Point out each leukocyte.
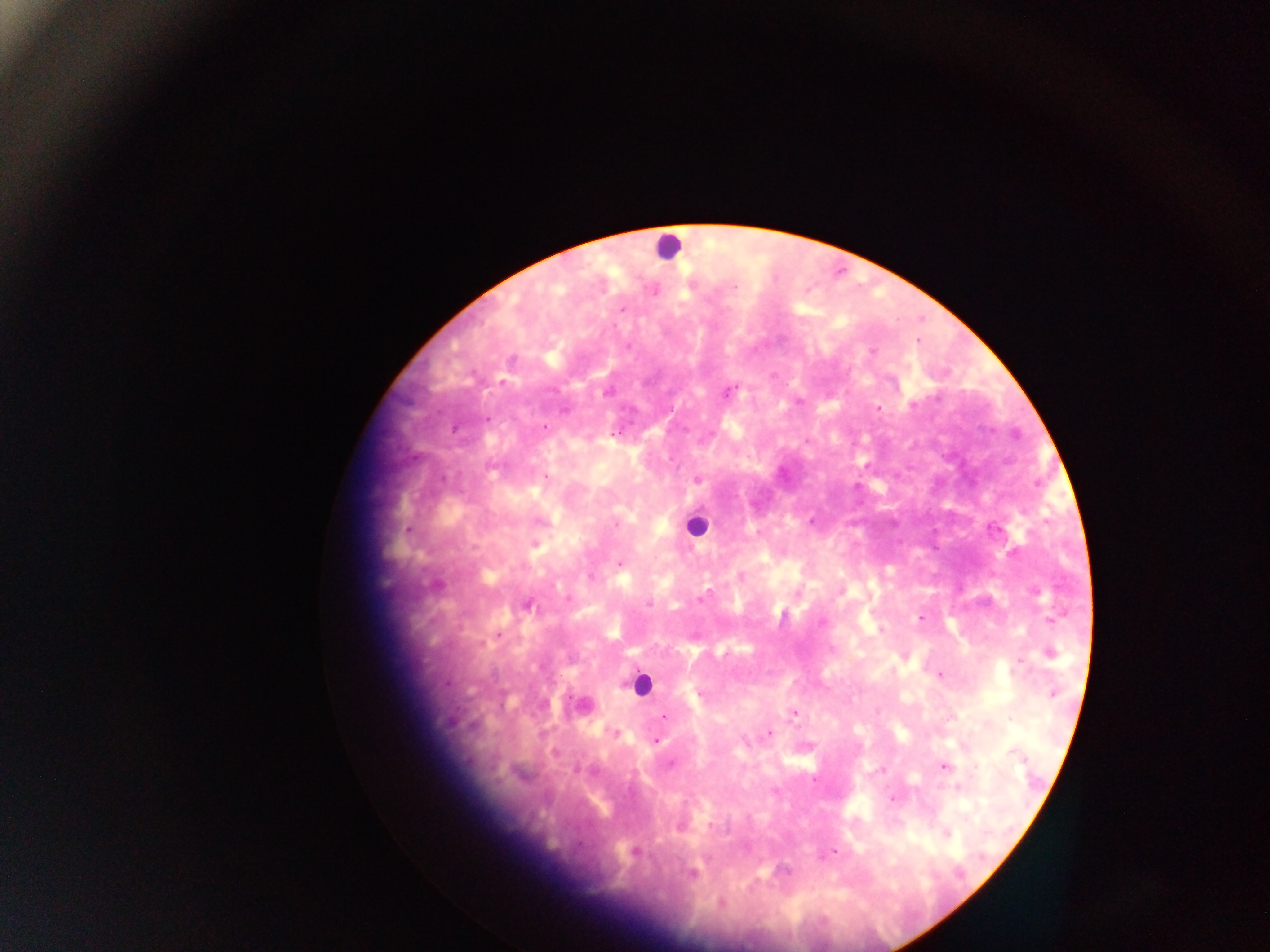
Approximate centers as (x, y) in pixels.
Leukocytes: (667, 246), (694, 526), (641, 683).

Summary:
  - Plasmodium parasite locations: (735, 287), (622, 309), (871, 351), (729, 391), (913, 405), (878, 408), (486, 419), (544, 428), (546, 477), (697, 480), (617, 523), (408, 529), (619, 564), (590, 577), (703, 597), (648, 604), (526, 605), (921, 618), (1051, 619), (822, 623), (498, 634), (1051, 653), (1020, 662), (940, 675), (699, 694), (1054, 694), (794, 713), (664, 715), (769, 733), (656, 740), (1014, 753), (670, 763), (944, 767), (882, 771), (958, 787), (892, 799), (711, 825), (948, 834), (635, 851), (834, 852), (692, 875), (722, 903)
  - Country: Ghana
  - Field of view: single
  - Preparation: thick blood smear
  - Image size: 1270×952 pixels
  - Capture: mobile-phone photograph through a microscope